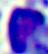

Summary:
  - Identification: leukocyte
  - Modality: micrograph
  - Magnification: 400x